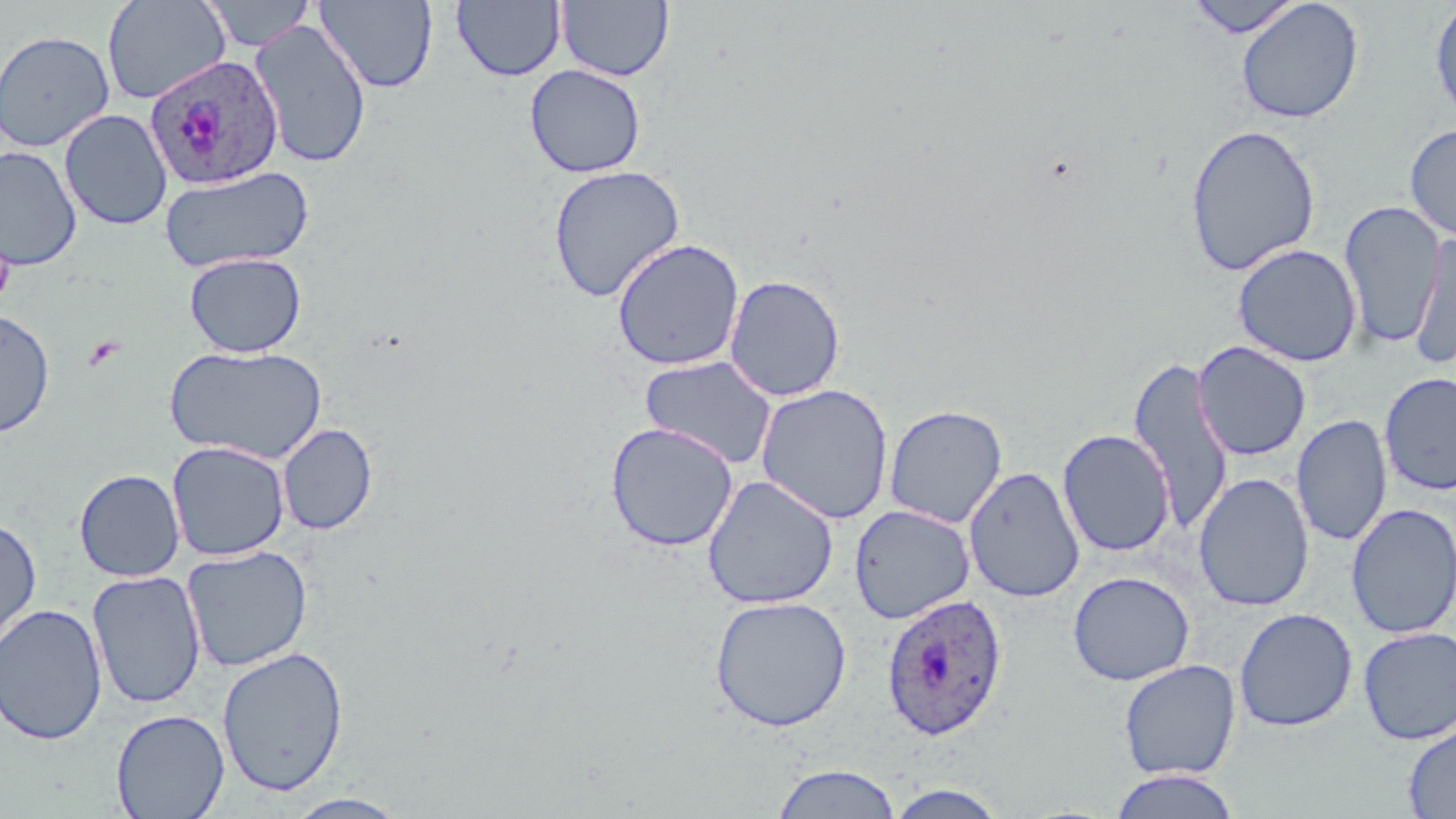

{
  "slide_level_diagnosis": "Plasmodium ovale",
  "platelet_locations": "approximate bounding boxes as (x1,y1)-(x2,y2) corner pairs in pixels: (82,335)-(125,371)",
  "image_size": "1456×819 pixels",
  "field_of_view": "one of a larger specimen",
  "magnification": "1000x",
  "plasmodium_ovale_infected_red_blood_cell_locations": "approximate bounding boxes as (x1,y1)-(x2,y2) corner pairs in pixels: (143,54)-(285,192), (881,593)-(1008,739)",
  "preparation": "thin blood smear",
  "uninfected_red_blood_cell_locations": "approximate bounding boxes as (x1,y1)-(x2,y2) corner pairs in pixels: (102,0)-(231,104), (205,0)-(315,52), (315,0)-(438,92), (557,0)-(674,82), (1186,0)-(1304,39), (451,1)-(567,82), (1236,1)-(1364,124), (1429,1)-(1456,126), (249,19)-(373,169), (0,29)-(116,153), (525,64)-(646,178), (59,108)-(173,231), (1185,123)-(1321,277), (1404,123)-(1456,242), (0,146)-(82,271), (548,164)-(686,303), (159,165)-(314,273), (1339,201)-(1446,349), (1410,232)-(1456,367), (611,238)-(745,371), (1232,243)-(1362,367), (184,252)-(306,358), (724,274)-(846,401), (0,309)-(55,438), (1193,341)-(1311,461), (165,344)-(327,464), (640,355)-(778,471), (1128,355)-(1235,534), (1379,372)-(1456,495), (756,383)-(894,524), (883,404)-(1008,528), (1291,415)-(1392,546), (605,421)-(739,552), (278,423)-(378,535), (1057,428)-(1175,558), (167,441)-(290,561), (964,466)-(1085,603), (74,468)-(185,582), (1194,473)-(1314,611), (702,474)-(839,609), (1346,503)-(1456,639), (849,505)-(975,623), (0,515)-(42,651), (182,545)-(312,672), (87,570)-(207,710), (1068,571)-(1194,686), (709,595)-(851,732), (0,603)-(107,745), (1234,608)-(1358,732), (1358,626)-(1456,744), (217,645)-(349,796), (1118,659)-(1241,780), (110,709)-(230,819), (1403,720)-(1456,818), (772,763)-(901,818), (1108,769)-(1242,819), (883,783)-(1010,819), (283,793)-(411,819)",
  "modality": "optical microscopy",
  "stain": "May-Grünwald-Giemsa"
}